Outline platelets.
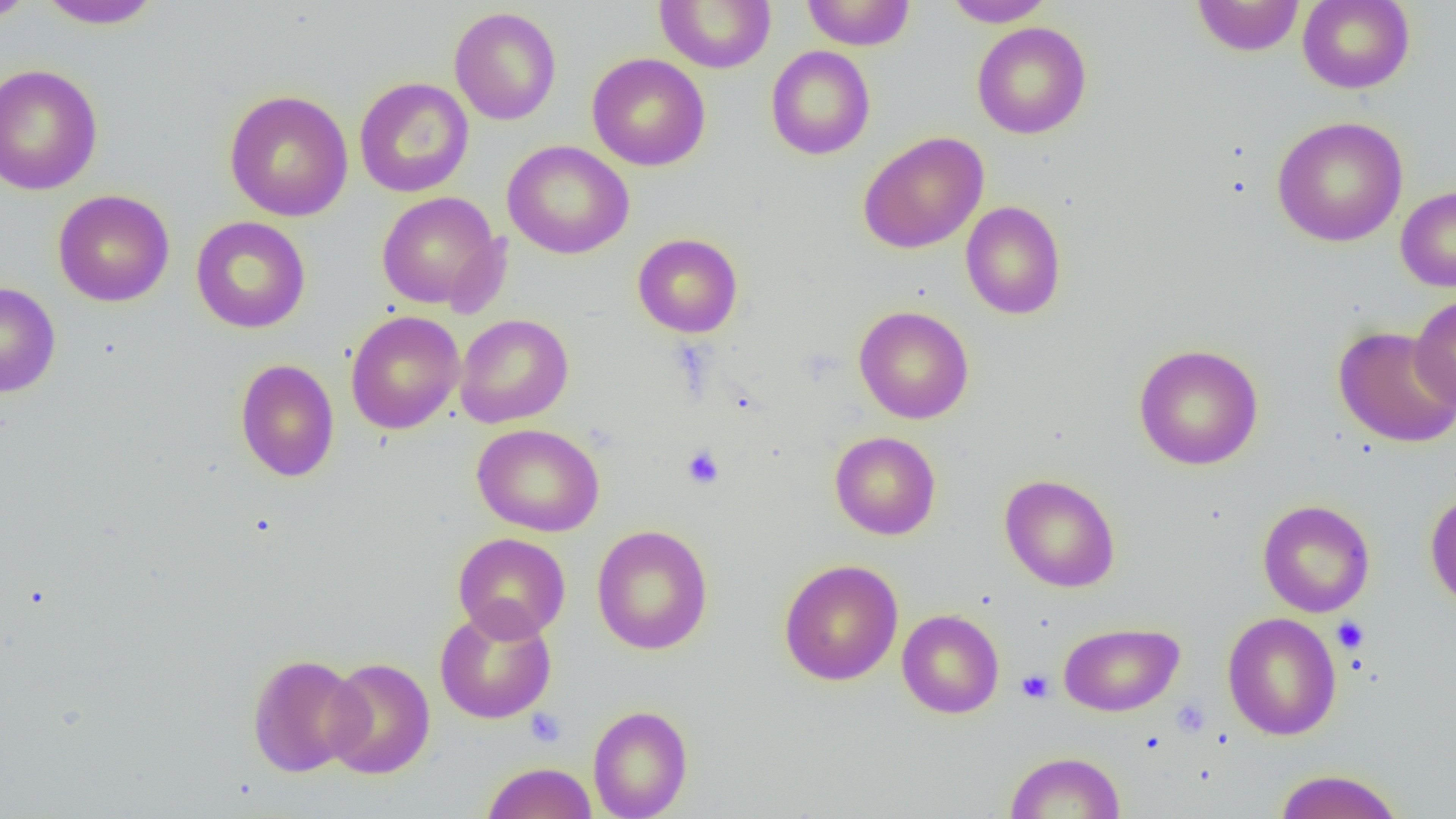
Approximate bounding boxes as named x1/y1/x2/y2 corners in pixels.
Platelets: (x1=681, y1=445, x2=724, y2=488), (x1=1331, y1=616, x2=1370, y2=653), (x1=1017, y1=669, x2=1054, y2=703), (x1=1171, y1=698, x2=1210, y2=739), (x1=525, y1=708, x2=566, y2=747).

slide_level_diagnosis: no evidence of blood parasites
field_of_view: single
preparation: thin blood film
uninfected_red_blood_cell_locations: 'approximate bounding boxes as named x1/y1/x2/y2 corners in pixels: (x1=1, y1=0, x2=37, y2=24), (x1=35, y1=0, x2=163, y2=30), (x1=654, y1=0, x2=776, y2=73), (x1=801, y1=0, x2=916, y2=50), (x1=943, y1=0, x2=1054, y2=27), (x1=1191, y1=0, x2=1305, y2=57), (x1=1297, y1=0, x2=1415, y2=94), (x1=449, y1=7, x2=561, y2=125), (x1=972, y1=22, x2=1092, y2=139), (x1=765, y1=45, x2=875, y2=160), (x1=587, y1=53, x2=710, y2=171), (x1=0, y1=63, x2=103, y2=195), (x1=353, y1=77, x2=474, y2=198), (x1=224, y1=89, x2=354, y2=222), (x1=1271, y1=116, x2=1408, y2=247), (x1=857, y1=131, x2=989, y2=254), (x1=502, y1=140, x2=634, y2=259), (x1=1396, y1=186, x2=1456, y2=291), (x1=52, y1=190, x2=174, y2=307), (x1=376, y1=191, x2=503, y2=311), (x1=960, y1=201, x2=1066, y2=320), (x1=190, y1=216, x2=310, y2=333), (x1=632, y1=233, x2=743, y2=338), (x1=0, y1=282, x2=61, y2=397), (x1=1410, y1=294, x2=1456, y2=409), (x1=853, y1=305, x2=975, y2=424), (x1=345, y1=310, x2=465, y2=435), (x1=454, y1=314, x2=573, y2=428), (x1=1333, y1=326, x2=1456, y2=450), (x1=1134, y1=343, x2=1264, y2=470), (x1=235, y1=358, x2=339, y2=482), (x1=473, y1=424, x2=603, y2=536), (x1=829, y1=431, x2=941, y2=540), (x1=1000, y1=474, x2=1121, y2=593), (x1=1425, y1=490, x2=1456, y2=612), (x1=1258, y1=499, x2=1375, y2=617), (x1=591, y1=525, x2=714, y2=655), (x1=452, y1=532, x2=571, y2=642), (x1=778, y1=559, x2=904, y2=686), (x1=434, y1=603, x2=557, y2=724), (x1=897, y1=609, x2=1004, y2=719), (x1=1222, y1=612, x2=1341, y2=741), (x1=1058, y1=622, x2=1185, y2=716), (x1=247, y1=653, x2=367, y2=777), (x1=323, y1=657, x2=436, y2=779), (x1=587, y1=704, x2=693, y2=819), (x1=1004, y1=751, x2=1126, y2=818), (x1=482, y1=762, x2=597, y2=819), (x1=1272, y1=768, x2=1405, y2=819)'
image_size: 1456×819 pixels
modality: optical microscopy
magnification: 1000x